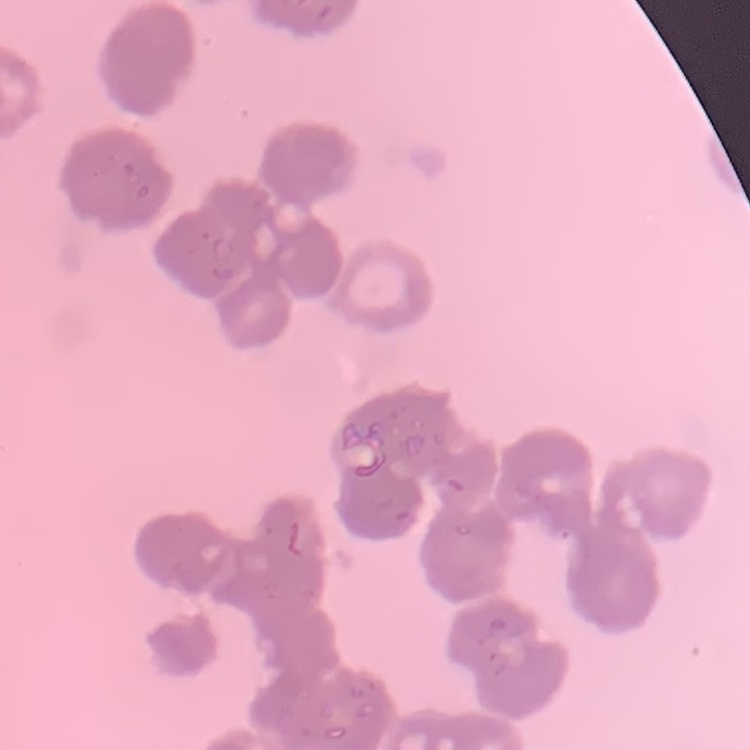 The erythrocytes show rouleaux formation. Square crop of a larger photomicrograph. Thin blood film. Field's or Giemsa stain.